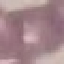

Result: no malaria parasites detected. Thin blood smear. Photographed with a smartphone camera at the microscope eyepiece. Giemsa-stained preparation. Cell patch, automatically extracted from a larger field of view and resized to 64 × 64 pixels.